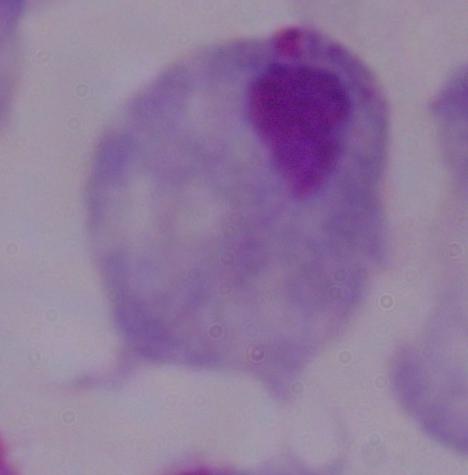

Captured at 1000x magnification. A trichomonad is seen. Photomicrograph.